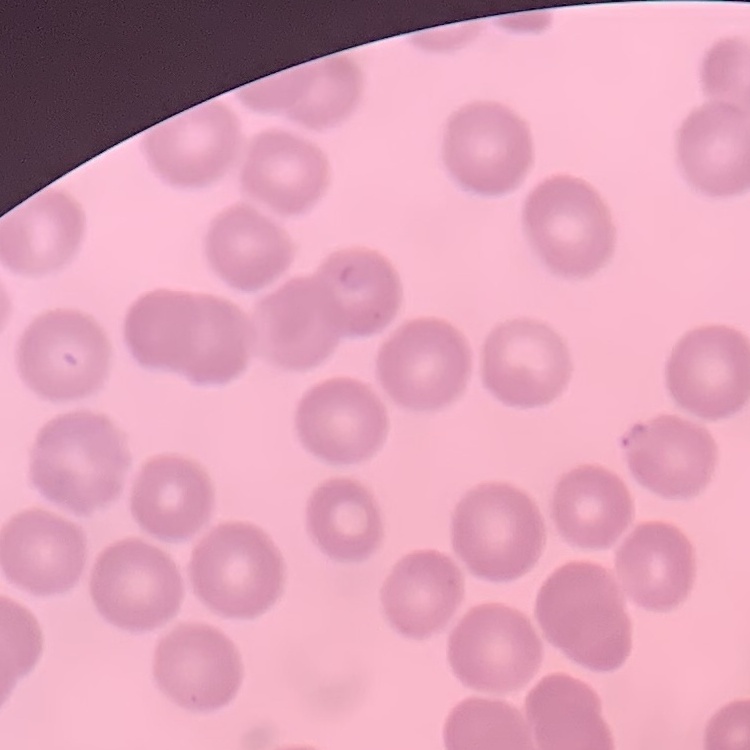

red blood cell morphology = no rouleaux formation
image type = one tile cut from a larger photomicrograph
preparation = thin blood smear
stain = Field's or Giemsa